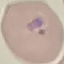

Summary:
  - Malaria status: parasitized
  - Image type: cell patch, automatically extracted from a larger field of view and resized to 64 × 64 pixels
  - Preparation: thin blood film
  - Capture: smartphone through the microscope eyepiece
  - Stain: Giemsa